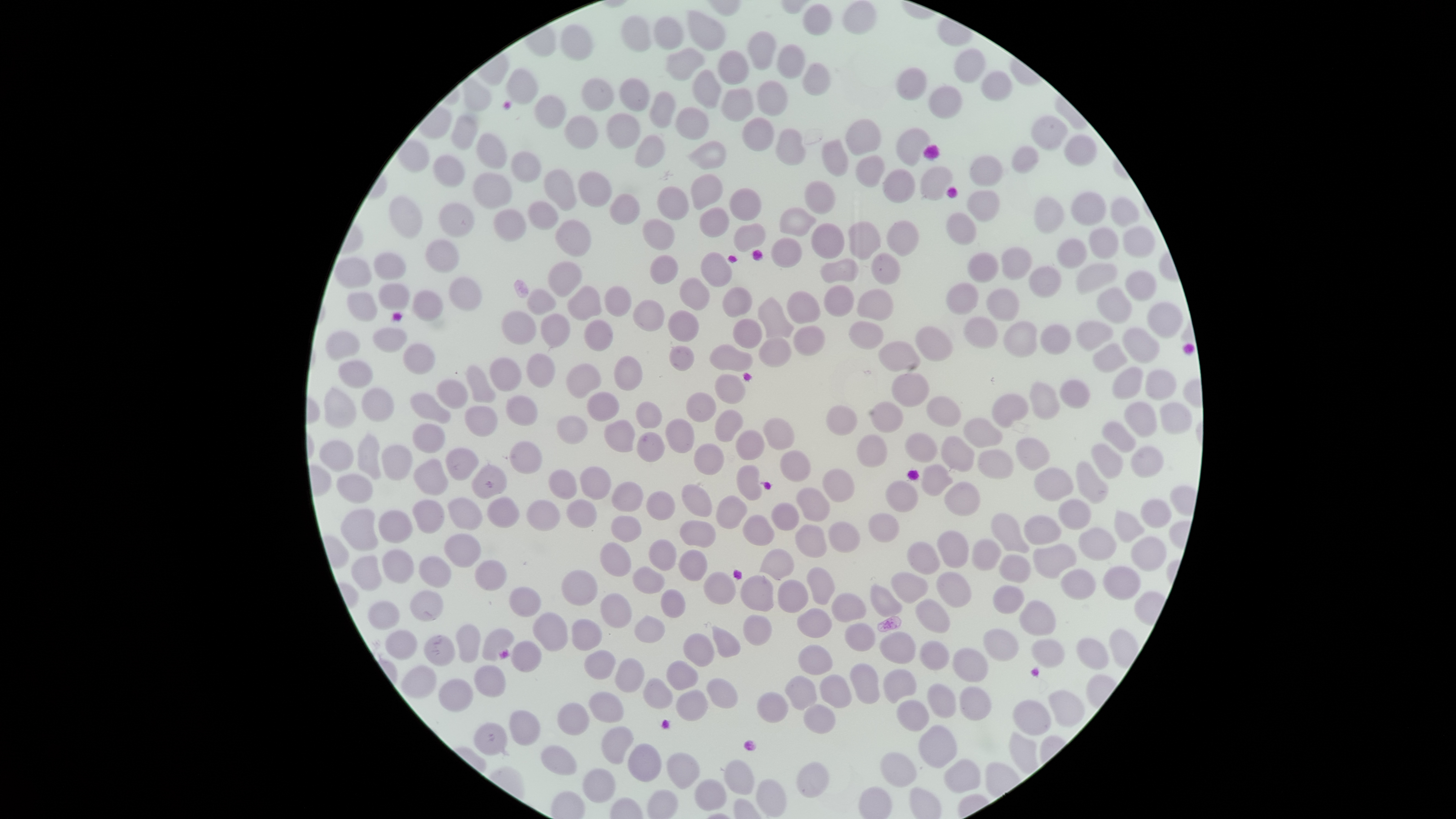
Approximate bounding boxes as {left, top, right, bottom} in pixels.
Summary:
  - Uninfected red blood cells: {843, 1, 875, 34}, {804, 4, 832, 35}, {686, 11, 725, 50}, {622, 16, 652, 53}, {655, 17, 684, 50}, {560, 24, 593, 59}, {748, 32, 776, 70}, {778, 44, 804, 79}, {668, 48, 705, 80}, {955, 48, 986, 83}, {719, 51, 749, 85}, {804, 64, 830, 97}, {897, 69, 927, 101}, {507, 70, 539, 103}, {692, 70, 721, 108}, {982, 71, 1013, 101}, {582, 77, 614, 111}, {619, 79, 650, 111}, {758, 81, 788, 116}, {929, 87, 961, 120}, {650, 92, 675, 128}, {535, 97, 566, 129}, {676, 106, 709, 138}, {608, 113, 640, 148}, {451, 114, 479, 149}, {563, 116, 597, 148}, {1032, 116, 1068, 151}, {743, 118, 774, 151}, {846, 119, 881, 154}, {896, 127, 930, 166}, {776, 129, 805, 164}, {477, 133, 508, 168}, {635, 136, 664, 167}, {1065, 136, 1096, 165}, {690, 140, 726, 170}, {823, 140, 848, 175}, {1011, 146, 1039, 174}, {513, 152, 541, 182}, {432, 155, 464, 186}, {969, 155, 1004, 186}, {858, 156, 885, 187}, {920, 167, 953, 201}, {544, 169, 577, 211}, {883, 169, 915, 203}, {578, 171, 612, 207}, {473, 173, 511, 208}, {692, 173, 723, 210}, {805, 181, 835, 213}, {656, 187, 689, 220}, {729, 189, 761, 220}, {968, 191, 999, 222}, {609, 193, 639, 225}, {1072, 193, 1106, 225}, {390, 197, 423, 238}, {1034, 197, 1063, 233}, {1109, 198, 1140, 226}, {529, 200, 558, 229}, {438, 204, 474, 237}, {780, 206, 816, 237}, {699, 207, 730, 237}, {495, 209, 526, 240}, {947, 213, 976, 245}, {643, 218, 675, 250}, {556, 220, 591, 257}, {887, 221, 917, 256}, {849, 222, 881, 259}, {735, 223, 765, 252}, {812, 223, 845, 258}, {1123, 225, 1155, 257}, {1090, 228, 1119, 259}, {772, 237, 802, 268}, {1057, 238, 1086, 269}, {425, 241, 459, 272}, {1002, 248, 1031, 278}, {701, 252, 732, 286}, {374, 253, 406, 280}, {871, 253, 900, 284}, {651, 255, 679, 283}, {969, 255, 998, 283}, {821, 258, 859, 283}, {335, 259, 371, 287}, {549, 262, 582, 296}, {1078, 263, 1117, 294}, {1029, 267, 1060, 298}, {1126, 270, 1156, 301}, {681, 276, 708, 310}, {450, 278, 481, 310}, {379, 282, 410, 311}, {949, 283, 978, 316}, {568, 285, 601, 322}, {823, 285, 853, 316}, {605, 286, 631, 316}, {723, 287, 751, 318}, {988, 288, 1019, 321}, {525, 289, 556, 314}, {1097, 289, 1133, 324}, {413, 290, 443, 320}, {859, 290, 893, 320}, {788, 291, 821, 322}, {348, 292, 377, 321}, {757, 298, 793, 338}, {633, 299, 664, 331}, {1147, 302, 1183, 338}, {501, 311, 536, 343}, {669, 311, 698, 342}, {542, 315, 569, 346}, {965, 317, 998, 348}, {733, 318, 763, 347}, {850, 319, 883, 350}, {583, 320, 613, 350}, {1004, 322, 1036, 356}, {1077, 322, 1113, 350}, {1041, 325, 1069, 353}, {794, 326, 823, 355}, {373, 327, 406, 351}, {916, 327, 952, 361}, {1123, 328, 1160, 363}, {326, 333, 360, 360}, {760, 339, 791, 367}, {878, 342, 920, 371}, {404, 343, 434, 375}, {711, 344, 753, 372}, {1094, 344, 1126, 372}, {669, 345, 694, 370}, {526, 354, 556, 387}, {490, 356, 520, 392}, {615, 357, 642, 389}, {338, 361, 373, 389}, {567, 364, 600, 398}, {467, 366, 495, 404}, {1115, 367, 1142, 400}, {1145, 370, 1176, 400}, {892, 373, 929, 406}, {714, 374, 746, 404}, {437, 380, 468, 409}, {1060, 380, 1090, 408}, {1030, 382, 1059, 418}, {325, 389, 356, 428}, {363, 389, 394, 421}, {410, 392, 452, 423}, {588, 392, 619, 421}, {687, 392, 716, 422}, {993, 393, 1029, 427}, {506, 395, 537, 425}, {927, 396, 961, 427}, {636, 401, 662, 429}, {1125, 401, 1158, 439}, {871, 402, 903, 432}, {1160, 402, 1191, 433}, {827, 405, 858, 435}, {466, 406, 498, 437}, {715, 410, 743, 441}, {556, 416, 588, 444}, {666, 418, 694, 454}, {764, 418, 794, 451}, {963, 418, 1002, 448}, {605, 420, 635, 452}, {1102, 422, 1136, 452}, {412, 424, 445, 453}, {734, 430, 764, 461}, {638, 432, 664, 462}, {357, 433, 381, 479}, {905, 434, 937, 462}, {858, 435, 887, 466}, {942, 436, 975, 471}, {1016, 438, 1050, 469}, {319, 441, 354, 471}, {510, 442, 542, 473}, {695, 443, 723, 474}, {382, 445, 412, 480}, {1091, 445, 1123, 479}, {1131, 446, 1163, 478}, {446, 447, 479, 480}, {977, 449, 1013, 479}, {780, 451, 811, 482}, {414, 460, 448, 495}, {1076, 461, 1108, 505}, {737, 464, 762, 501}, {473, 465, 506, 499}, {923, 465, 953, 495}, {580, 467, 611, 499}, {1035, 467, 1074, 501}, {824, 468, 855, 502}, {547, 470, 576, 499}, {338, 474, 373, 503}, {944, 480, 979, 515}, {612, 481, 642, 511}, {885, 482, 918, 512}, {683, 484, 712, 517}, {797, 488, 829, 520}, {645, 491, 674, 520}, {716, 494, 748, 528}, {489, 497, 518, 528}, {449, 498, 483, 530}, {414, 499, 443, 533}, {568, 499, 596, 527}, {1060, 499, 1091, 530}, {529, 500, 558, 531}, {1141, 500, 1171, 529}, {771, 503, 799, 530}, {342, 509, 378, 551}, {1115, 510, 1144, 542}, {379, 511, 412, 542}, {869, 511, 900, 542}, {992, 513, 1030, 552}, {743, 515, 775, 546}, {1023, 515, 1061, 543}, {611, 516, 643, 541}, {680, 520, 716, 547}, {828, 522, 859, 552}, {796, 525, 826, 557}, {1080, 527, 1116, 560}, {937, 530, 969, 567}, {444, 535, 481, 568}, {1132, 537, 1166, 570}, {649, 538, 677, 570}, {971, 540, 1002, 571}, {907, 541, 939, 574}, {1034, 542, 1076, 578}, {600, 543, 630, 576}, {759, 548, 796, 580}, {680, 549, 707, 582}, {382, 550, 413, 584}, {999, 554, 1031, 582}, {352, 555, 382, 590}, {420, 556, 452, 588}, {475, 561, 507, 590}, {1103, 566, 1139, 601}, {634, 567, 664, 594}, {807, 568, 835, 607}, {563, 570, 596, 603}, {937, 570, 971, 605}, {1061, 570, 1094, 600}, {704, 572, 734, 605}, {892, 572, 928, 603}, {741, 576, 774, 611}, {780, 581, 809, 613}, {868, 584, 902, 616}, {509, 586, 541, 616}, {994, 586, 1023, 616}, {659, 589, 685, 617}, {409, 590, 443, 622}, {600, 593, 632, 629}, {832, 594, 866, 621}, {915, 599, 950, 632}, {1019, 599, 1055, 636}, {369, 602, 398, 630}, {799, 608, 832, 638}, {535, 613, 569, 651}, {742, 615, 772, 646}, {635, 617, 664, 643}, {573, 619, 602, 652}, {845, 624, 875, 651}, {457, 625, 481, 663}, {482, 627, 515, 661}, {712, 627, 741, 657}, {984, 628, 1018, 659}, {386, 629, 418, 659}, {882, 632, 915, 665}, {684, 633, 713, 667}, {424, 636, 455, 667}, {1076, 638, 1108, 669}, {1031, 640, 1065, 667}, {920, 641, 949, 671}, {512, 642, 542, 672}, {799, 644, 833, 675}, {952, 649, 988, 681}, {585, 650, 616, 679}, {616, 658, 645, 693}, {667, 661, 698, 690}, {849, 662, 880, 705}, {475, 666, 505, 698}, {402, 667, 437, 698}, {884, 670, 916, 702}, {786, 675, 816, 709}, {820, 675, 851, 707}, {707, 678, 738, 708}, {440, 680, 474, 712}, {643, 680, 673, 708}, {927, 684, 956, 718}, {961, 687, 991, 721}, {676, 689, 707, 721}, {1050, 690, 1084, 725}, {588, 692, 623, 723}, {759, 692, 787, 722}, {898, 700, 929, 732}, {1013, 701, 1051, 734}, {558, 702, 589, 735}, {805, 706, 835, 732}, {508, 710, 540, 745}, {475, 723, 507, 755}, {920, 723, 957, 769}, {602, 727, 634, 764}, {629, 743, 663, 782}, {542, 746, 577, 775}, {881, 752, 916, 788}, {667, 753, 699, 788}, {946, 759, 982, 794}, {724, 760, 755, 794}, {797, 762, 828, 796}, {584, 768, 615, 802}, {695, 779, 727, 811}, {757, 780, 787, 816}
  - Capture: smartphone photograph through the microscope eyepiece
  - Preparation: thin blood smear
  - Field of view: single
  - Stain: Giemsa
  - Image size: 1456×819 pixels
  - Presence: no malaria parasites detected
  - Visible region: circular